Outline each Plasmodium falciparum-infected red blood cell.
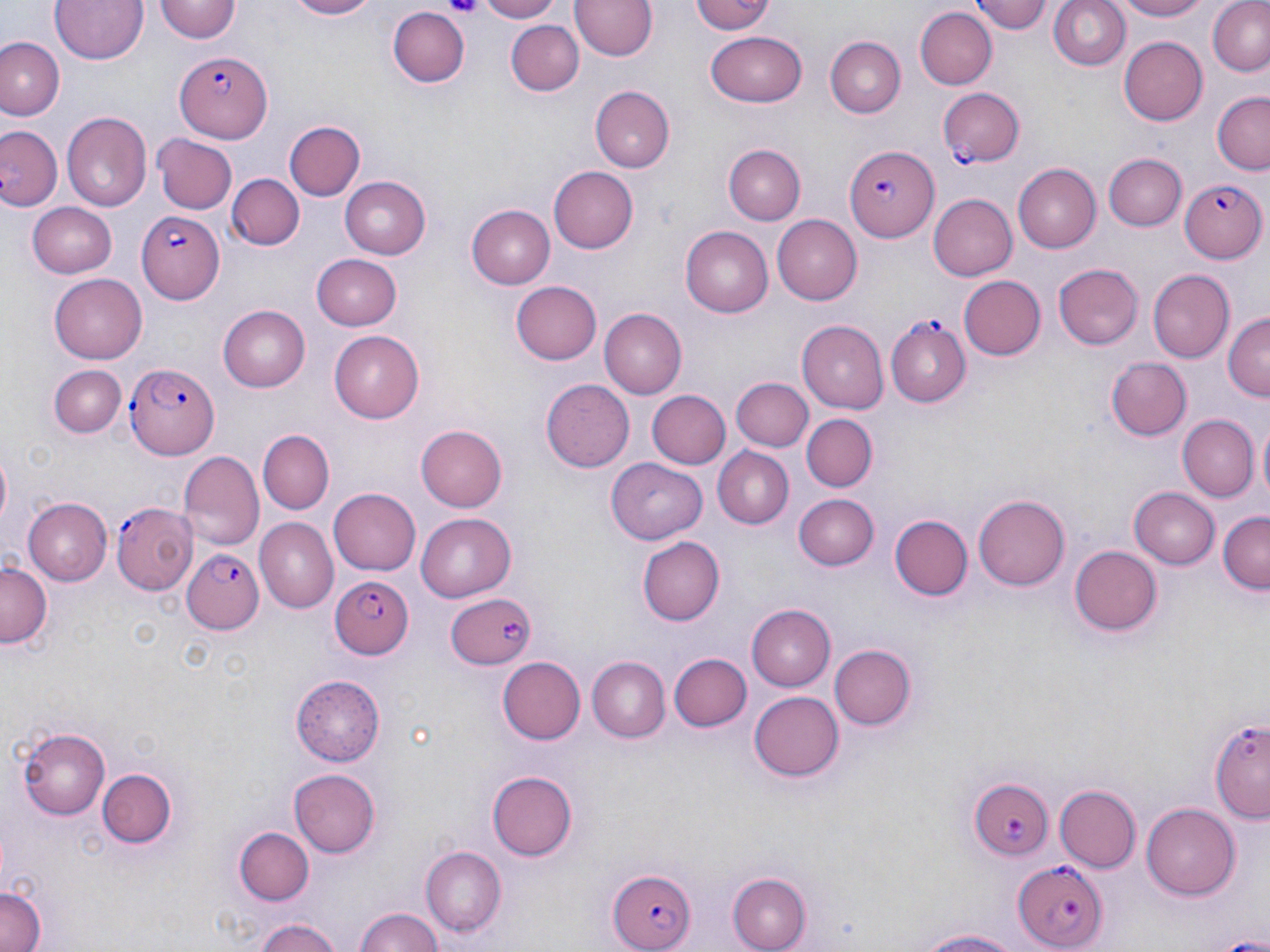

Approximate bounding boxes as (x1, y1, x2, y2) in pixels.
Plasmodium falciparum-infected red blood cells: (174, 46, 273, 145), (938, 88, 1024, 166), (845, 143, 940, 244), (1180, 180, 1266, 262), (138, 210, 225, 302), (883, 317, 971, 407), (125, 361, 219, 459), (112, 502, 196, 591), (181, 548, 264, 635), (328, 575, 415, 659), (443, 590, 538, 667), (965, 777, 1055, 861), (1010, 859, 1108, 951), (605, 869, 695, 952).

Platelet locations: (445, 0, 483, 20). Uninfected red blood cell locations: (49, 0, 150, 65), (278, 0, 379, 20), (475, 0, 561, 22), (692, 0, 775, 36), (975, 0, 1053, 34), (1047, 0, 1130, 73), (1114, 0, 1213, 21), (1208, 0, 1270, 79), (154, 1, 241, 44), (571, 1, 657, 63), (383, 5, 470, 88), (916, 7, 996, 89), (506, 19, 583, 97), (707, 32, 806, 108), (1, 36, 63, 119), (825, 36, 905, 116), (1119, 36, 1208, 125), (591, 86, 672, 172), (1211, 93, 1269, 174), (62, 111, 151, 209), (285, 120, 365, 199), (0, 126, 62, 212), (154, 134, 237, 214), (727, 146, 805, 225), (1105, 154, 1187, 230), (1011, 164, 1100, 252), (549, 166, 639, 253), (228, 173, 302, 251), (340, 176, 430, 258), (929, 194, 1017, 281), (28, 201, 118, 276), (469, 204, 557, 289), (771, 215, 862, 304), (679, 227, 773, 318), (311, 254, 402, 329), (1054, 263, 1143, 349), (1148, 270, 1235, 361), (49, 273, 149, 363), (959, 275, 1046, 361), (513, 279, 602, 364), (218, 305, 310, 392), (600, 309, 686, 398), (1224, 314, 1269, 403), (797, 321, 889, 413), (327, 330, 425, 423), (1105, 357, 1192, 439), (50, 364, 126, 437), (730, 377, 811, 453), (544, 379, 635, 472), (647, 390, 731, 470), (800, 414, 875, 492), (1177, 415, 1258, 501), (418, 423, 507, 513), (257, 430, 334, 514), (711, 447, 795, 529), (178, 449, 263, 551), (607, 459, 706, 543), (1131, 485, 1221, 568), (328, 488, 419, 576), (795, 493, 878, 571), (974, 494, 1070, 590), (24, 497, 112, 584), (1217, 511, 1270, 593), (417, 513, 517, 602), (888, 515, 970, 600), (254, 519, 336, 612), (638, 536, 724, 626), (1070, 545, 1161, 636), (0, 559, 52, 646), (746, 605, 834, 692), (829, 643, 915, 732), (669, 652, 750, 731), (496, 656, 586, 744), (586, 656, 669, 743), (291, 675, 386, 767), (749, 690, 844, 784), (1207, 715, 1270, 824), (17, 728, 109, 818), (97, 767, 175, 846), (292, 768, 380, 858), (488, 769, 578, 859), (1054, 784, 1141, 871), (1141, 802, 1241, 899), (235, 827, 312, 905), (420, 846, 507, 937), (726, 873, 811, 952), (0, 883, 44, 952), (352, 907, 445, 952), (252, 917, 344, 952), (908, 925, 1037, 950). Slide-level diagnosis: Plasmodium falciparum. 1000x magnification. Thin blood film. Single field of view. May-Grünwald-Giemsa stain. Image is 1270×952 pixels. Light microscopy.